State the preparation type.
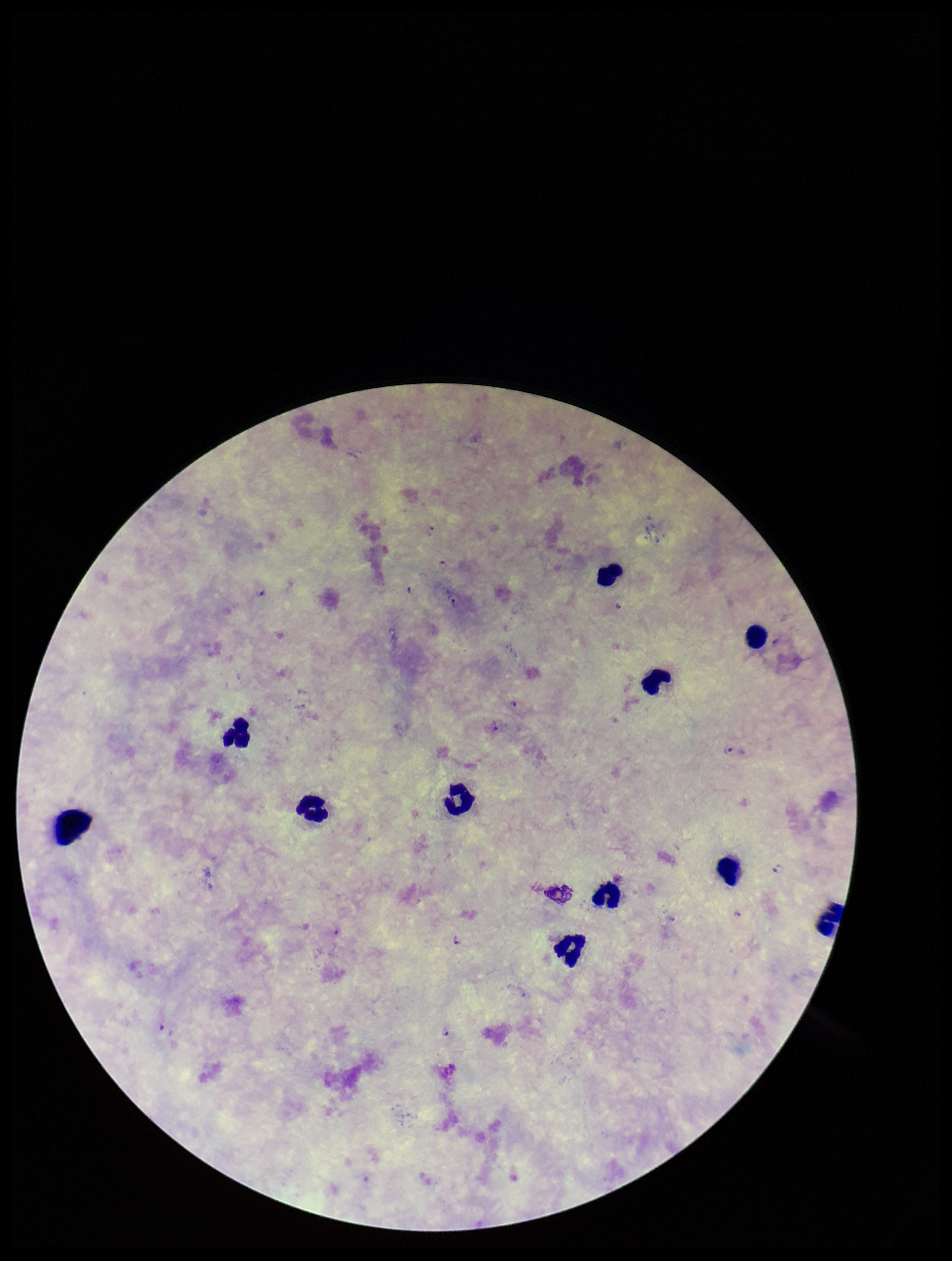
Thick.

Plasmodium parasites: detected. Parasite count: 8. Leukocyte count: 11. One field from this slide. Giemsa stain. Image is 952×1261 pixels. Species reported for this patient: Plasmodium falciparum. Patient malaria status: infected. Smartphone photograph taken through the eyepiece of a microscope.